Identify the parasite.
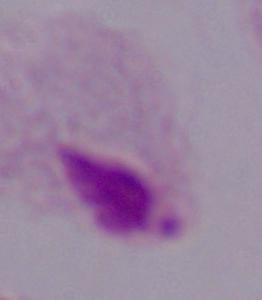

This is a trichomonad.

Summary:
  - Modality: micrograph
  - Magnification: 1000x